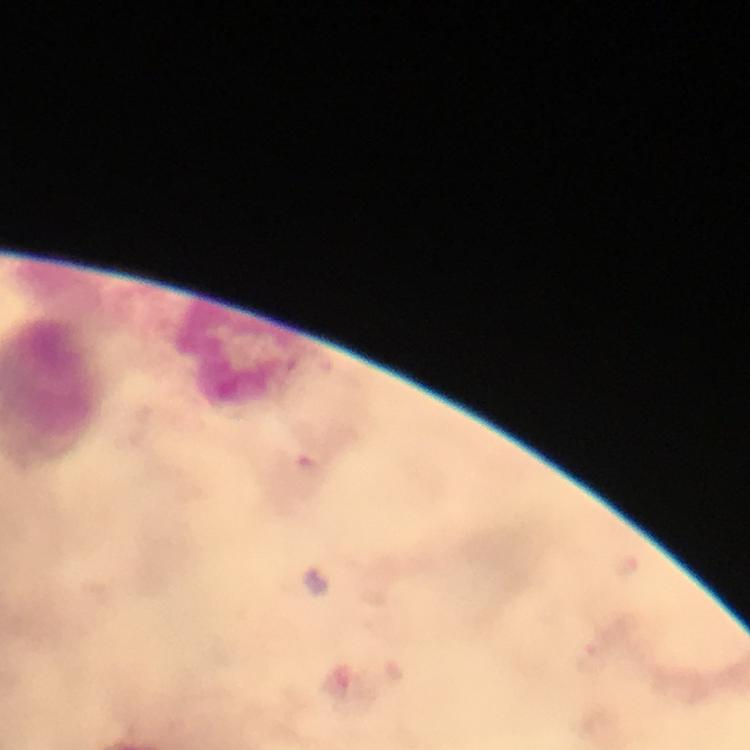

Approximate centers as {x, y} in pixels. Leukocyte locations: {238, 354}. At 100x magnification. Photographed through the microscope with a smartphone camera. Thick blood film. Image is 750×750 pixels. Giemsa-stained preparation. A crop from one field of view. Plasmodium parasites: none seen. Immersion oil applied. From a diagnostic examination for malaria.